State which cell type is depicted.
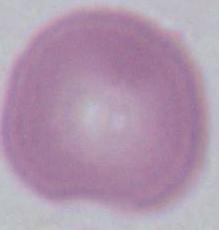
An erythrocyte.

magnification = 1000x
modality = micrograph